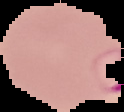

image type = cell region segmented out of the field of view; surrounding area masked to black
result = malaria parasites detected
preparation = thin blood smear
image size = 124×112 pixels